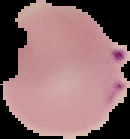
image_size: 130×139 pixels
image_type: cell region segmented out of the field of view; surrounding area masked to black
malaria_status: parasitized
preparation: thin blood smear